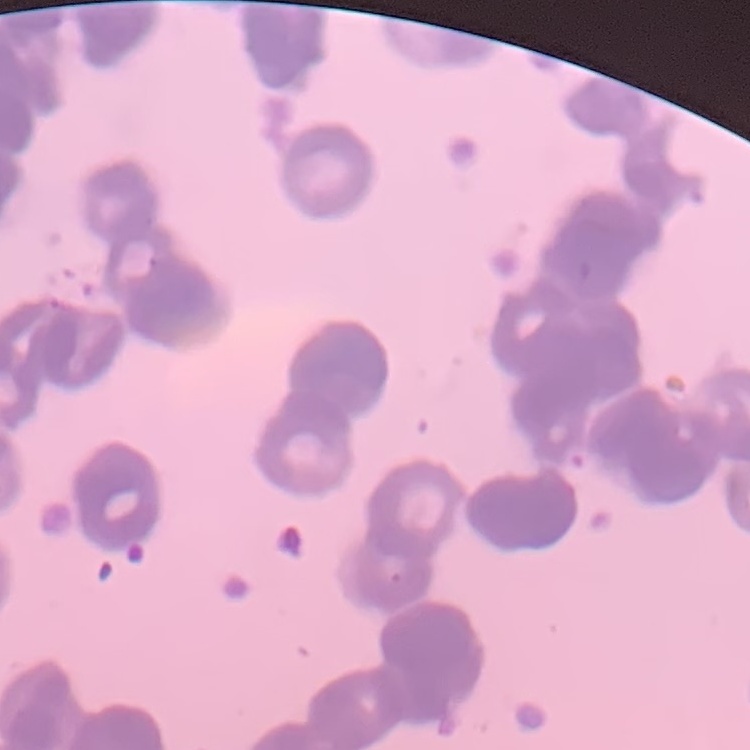

Summary:
  - Red blood cell morphology: rouleaux formation
  - Stain: Field's or Giemsa
  - Preparation: thin blood smear
  - Image type: square crop of a larger photomicrograph